Point out each leukocyte.
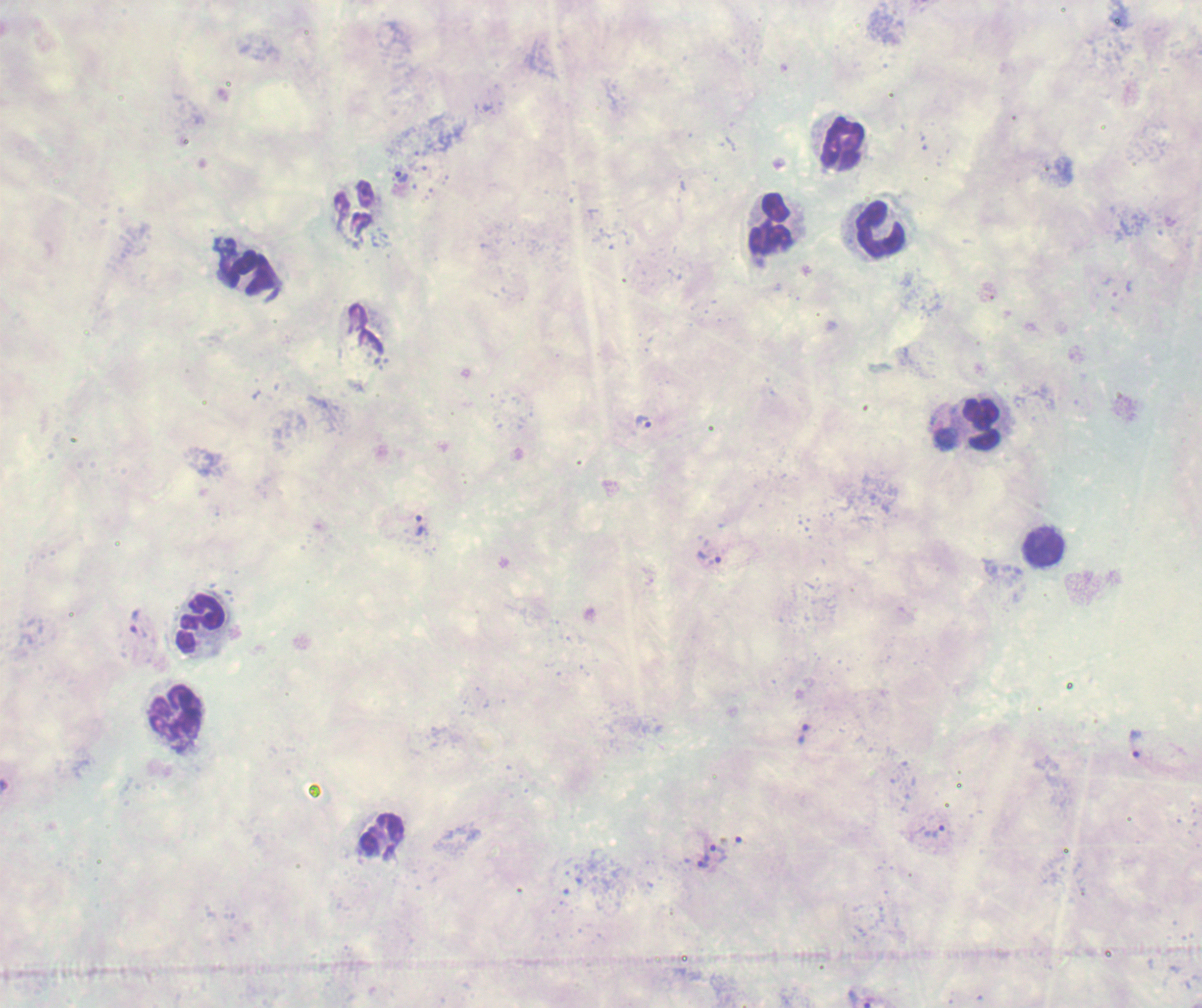
Approximate object centers, in pixels from the top-left corner.
Leukocytes: (x=839, y=142), (x=770, y=228), (x=881, y=229), (x=252, y=274), (x=982, y=423), (x=1044, y=546), (x=197, y=623), (x=174, y=717), (x=377, y=833).

Approximate object centers, in pixels from the top-left corner. Trophozoite locations: (x=400, y=176), (x=643, y=422), (x=420, y=525), (x=709, y=558), (x=134, y=620), (x=803, y=733), (x=1136, y=744), (x=934, y=830), (x=717, y=851), (x=705, y=862), (x=862, y=999). 100x magnification. Thick blood film. One field from this slide. Image is 1202×1008 pixels. Background quality: unsatisfactory. Previously used in a real diagnosis. Result: Plasmodium parasites identified. Romanowsky stain.